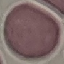
result = no malaria parasites seen
preparation = thin smear
stain = Giemsa
image type = cell patch, automatically extracted from a larger field of view and resized to 64 × 64 pixels
capture = smartphone camera at the microscope eyepiece